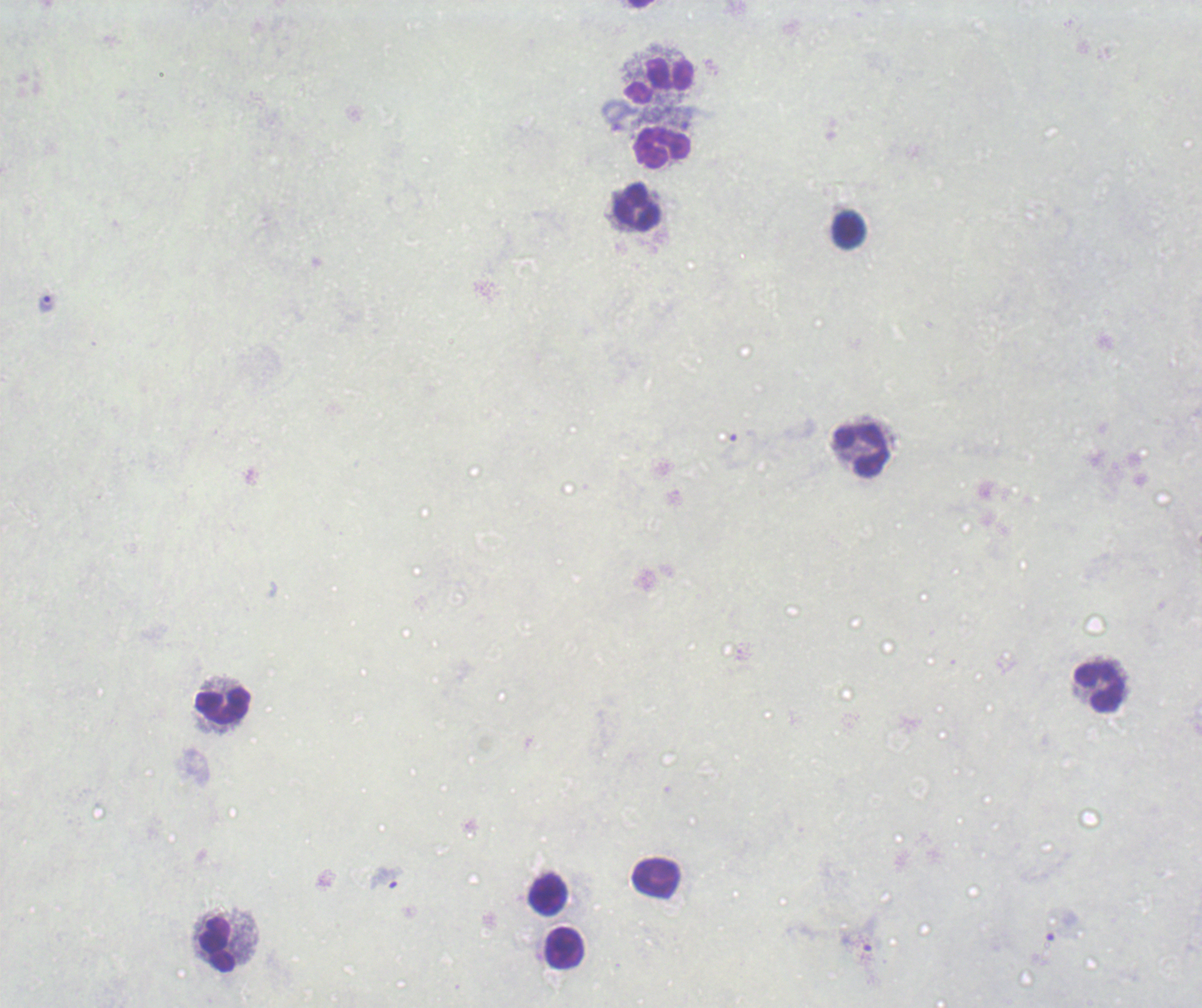

Approximate centers as [x, y] in pixels.
Summary:
  - Trophozoite locations: [46, 305], [385, 878]
  - Leukocyte locations: [660, 80], [661, 147], [635, 207], [849, 229], [861, 450], [1097, 687], [222, 707], [656, 877], [548, 895], [218, 944], [565, 947]
  - Field of view: single
  - Result: Plasmodium parasites detected
  - Image size: 1202×1008 pixels
  - Magnification: 100x
  - Preparation: thick blood film
  - Stain: Romanowsky
  - Background quality: poor
  - Context: previously used in an actual diagnosis